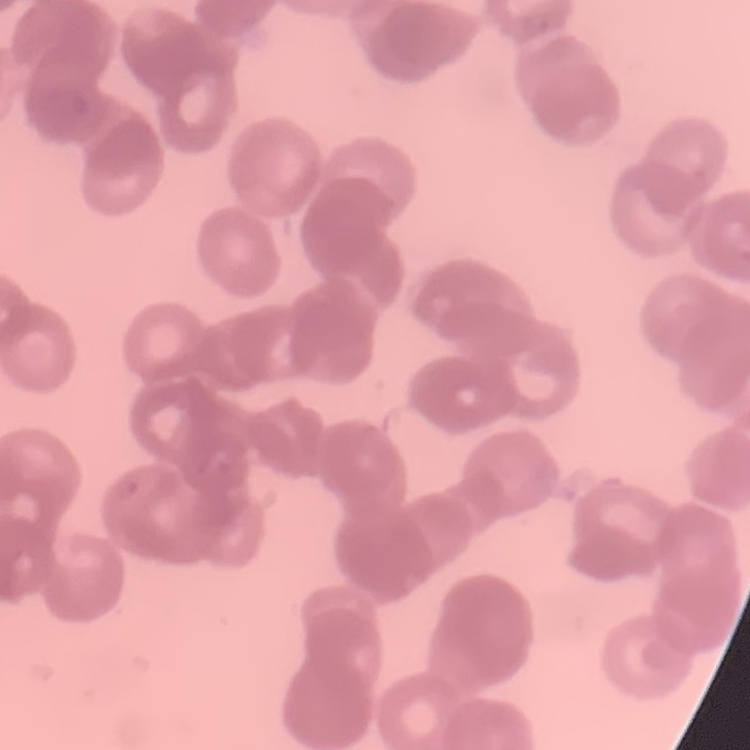
erythrocyte morphology = rouleaux formation
image type = square crop of a larger photomicrograph
stain = Field's or Giemsa
preparation = thin blood smear